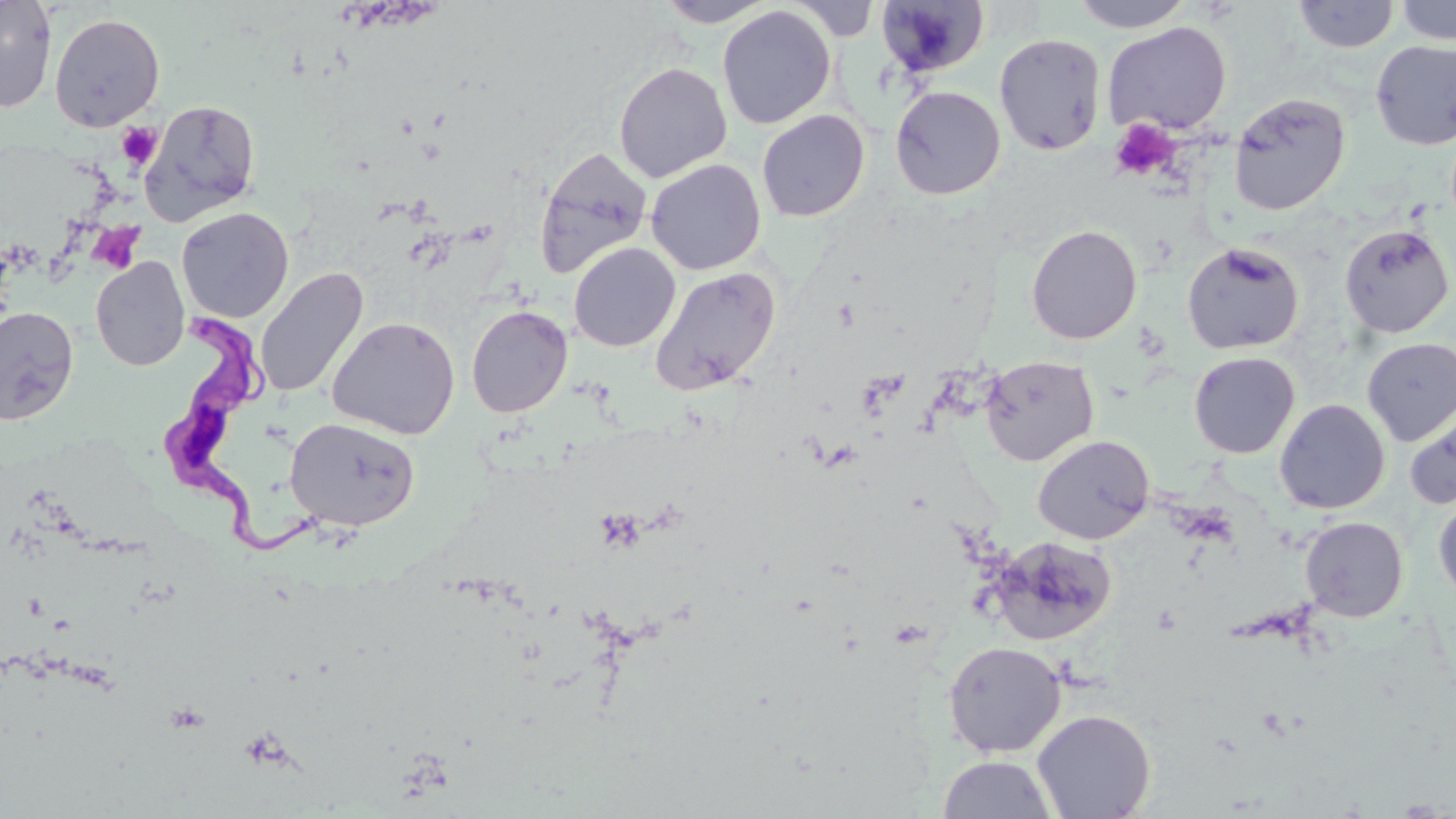

{
  "slide_level_diagnosis": "Trypanosoma brucei",
  "modality": "light microscopy",
  "magnification": "1000x",
  "field_of_view": "single",
  "uninfected_red_blood_cell_locations": "approximate bounding boxes as (x1, y1, x2, y2) in pixels: (0, 0, 58, 113), (654, 0, 775, 27), (789, 0, 882, 41), (1068, 0, 1195, 32), (1293, 0, 1400, 53), (1395, 0, 1456, 45), (874, 1, 990, 79), (718, 5, 836, 129), (49, 13, 165, 131), (1102, 21, 1232, 136), (994, 33, 1107, 157), (1370, 40, 1456, 150), (613, 62, 732, 183), (890, 86, 1005, 200), (1227, 91, 1351, 216), (140, 100, 261, 225), (757, 110, 870, 222), (534, 145, 653, 280), (646, 159, 766, 275), (176, 207, 294, 323), (1339, 223, 1454, 339), (1026, 224, 1143, 345), (1182, 241, 1305, 355), (569, 242, 680, 352), (91, 258, 190, 371), (649, 266, 782, 395), (255, 268, 369, 398), (0, 305, 79, 426), (466, 305, 573, 418), (327, 316, 461, 440), (1361, 337, 1456, 447), (1188, 351, 1300, 458), (980, 356, 1099, 466), (1274, 398, 1390, 514), (1404, 402, 1456, 512), (285, 418, 420, 532), (1032, 434, 1155, 544), (1433, 498, 1456, 605), (1300, 516, 1408, 622), (989, 536, 1117, 645), (943, 640, 1066, 757), (1032, 709, 1156, 818), (936, 754, 1057, 818)",
  "trypanosoma_brucei_locations": "approximate bounding boxes as (x1, y1, x2, y2) in pixels: (158, 303, 322, 558)",
  "stain": "May-Grünwald-Giemsa",
  "preparation": "thin blood smear",
  "platelet_locations": "approximate bounding boxes as (x1, y1, x2, y2) in pixels: (1110, 118, 1179, 181), (116, 122, 162, 169), (87, 221, 145, 274), (595, 508, 645, 552)",
  "image_size": "1456×819 pixels"
}